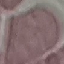

result: negative for malaria parasites
capture: smartphone camera at the microscope eyepiece
preparation: thin smear
stain: Giemsa
image_type: cell patch, automatically extracted from a larger field of view and resized to 64 × 64 pixels